Assess this cell for malaria.
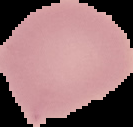

Uninfected.

image type = cell region segmented out of the field of view; surrounding area masked to black
image size = 133×127 pixels
preparation = thin blood film